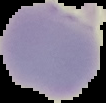 The area outside the segmented cell region is set to black. Image is 106×103 pixels. From a thin blood smear. Result: malaria parasites identified.